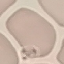

malaria status = uninfected
stain = Giemsa
capture = smartphone camera at the microscope eyepiece
preparation = thin blood smear
image type = automatically extracted cell patch, resized to 64 × 64 pixels